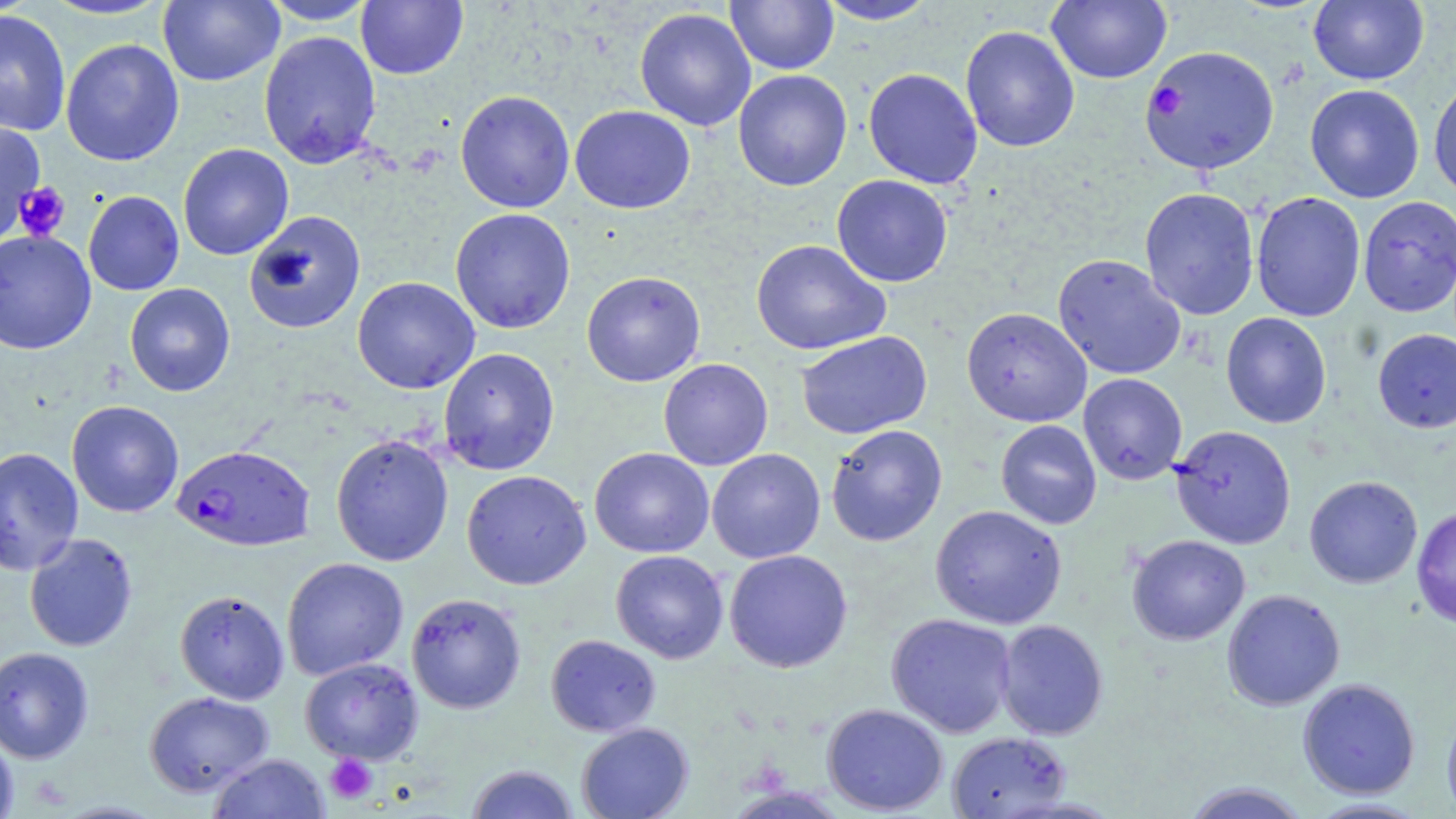
Approximate bounding boxes as [x1, y1, x2, y2] in pixels. Uninfected red blood cell locations: [40, 0, 173, 21], [159, 0, 284, 86], [259, 0, 378, 25], [1046, 0, 1172, 84], [1309, 0, 1429, 85], [356, 1, 468, 80], [725, 1, 839, 74], [816, 1, 938, 25], [634, 7, 756, 131], [0, 9, 71, 137], [960, 25, 1080, 153], [259, 31, 381, 169], [60, 39, 184, 166], [863, 68, 983, 189], [733, 69, 852, 191], [1428, 76, 1456, 201], [1304, 84, 1424, 203], [455, 90, 575, 213], [570, 105, 695, 214], [0, 121, 45, 242], [177, 143, 294, 260], [832, 174, 953, 287], [1139, 187, 1260, 320], [1239, 190, 1344, 430], [83, 191, 184, 295], [1250, 191, 1366, 322], [1357, 196, 1456, 317], [450, 208, 576, 333], [243, 210, 366, 334], [0, 229, 96, 354], [751, 239, 890, 356], [1053, 253, 1186, 380], [581, 270, 706, 387], [352, 276, 480, 394], [124, 283, 235, 397], [961, 307, 1092, 427], [1221, 312, 1332, 428], [1372, 329, 1456, 433], [796, 330, 932, 439], [438, 347, 560, 475], [658, 358, 773, 471], [1078, 373, 1187, 485], [66, 400, 184, 517], [995, 419, 1102, 529], [825, 424, 948, 546], [1170, 424, 1296, 549], [331, 434, 454, 567], [0, 447, 84, 576], [589, 448, 714, 558], [707, 448, 825, 563], [461, 469, 591, 590], [1304, 476, 1422, 589], [930, 505, 1067, 629], [1411, 507, 1456, 629], [24, 533, 138, 652], [1127, 534, 1250, 645], [724, 549, 853, 673], [610, 550, 729, 664], [281, 557, 409, 680], [1222, 589, 1345, 710], [174, 590, 290, 704], [406, 592, 526, 713], [886, 613, 1016, 738], [995, 620, 1109, 740], [545, 634, 661, 737], [0, 646, 94, 763], [300, 657, 423, 765], [1297, 678, 1420, 799], [143, 690, 275, 797], [822, 702, 949, 816], [1442, 704, 1456, 819], [575, 722, 693, 819], [0, 728, 19, 819], [946, 731, 1072, 818], [209, 753, 330, 818], [465, 763, 580, 819], [1180, 782, 1313, 819], [723, 786, 851, 818], [1305, 798, 1432, 818]. Plasmodium falciparum-infected red blood cell locations: [1139, 45, 1279, 175], [171, 444, 315, 551]. Platelet locations: [15, 182, 71, 241], [325, 755, 378, 804]. Slide-level diagnosis: Plasmodium falciparum. Single field of view. Image is 1456×819 pixels. Thin blood film. Captured at 1000x magnification. Light microscopy. May-Grünwald-Giemsa stain.